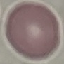
Summary:
  - Malaria status: uninfected
  - Capture: smartphone camera at the microscope eyepiece
  - Image type: cell patch, automatically extracted from a larger field of view and resized to 64 × 64 pixels
  - Stain: Giemsa
  - Preparation: thin smear